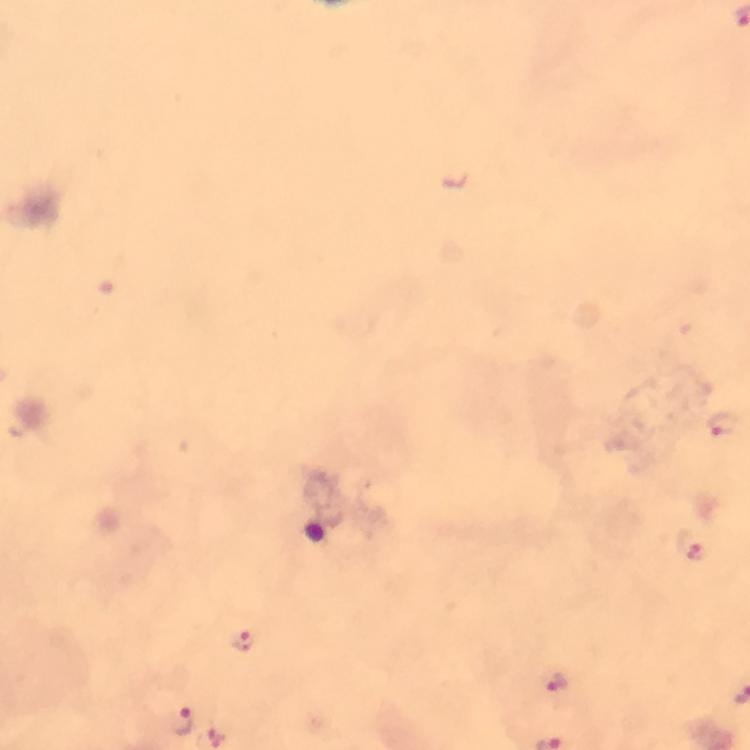
Approximate centers as (x, y) in pixels. Plasmodium parasite locations: (723, 423), (695, 551), (244, 640), (557, 681), (182, 722). Image is 750×750 pixels. From a diagnostic examination for malaria. A crop from one field of view. Immersion oil applied. 100x magnification. Giemsa-stained preparation. Thick blood film. Smartphone photograph taken through a microscope.